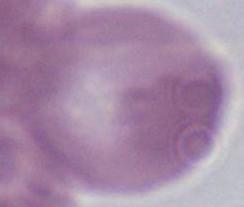

identification = red blood cell
magnification = 1000x
modality = photomicrograph